Assess the morphology of the erythrocytes.
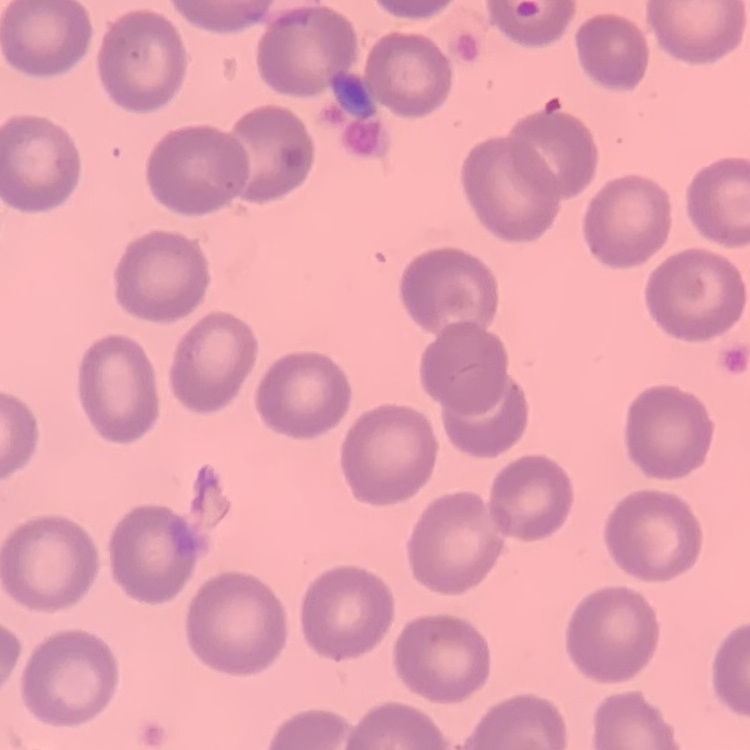
No rouleaux formation.

preparation = thin peripheral smear
image type = square crop of a larger photomicrograph
stain = Field's or Giemsa